Assess this cell for malaria.
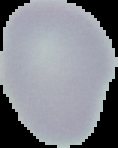
Uninfected.

{
  "preparation": "thin blood film",
  "image_size": "118×148 pixels",
  "image_type": "segmented cell region on a black background"
}